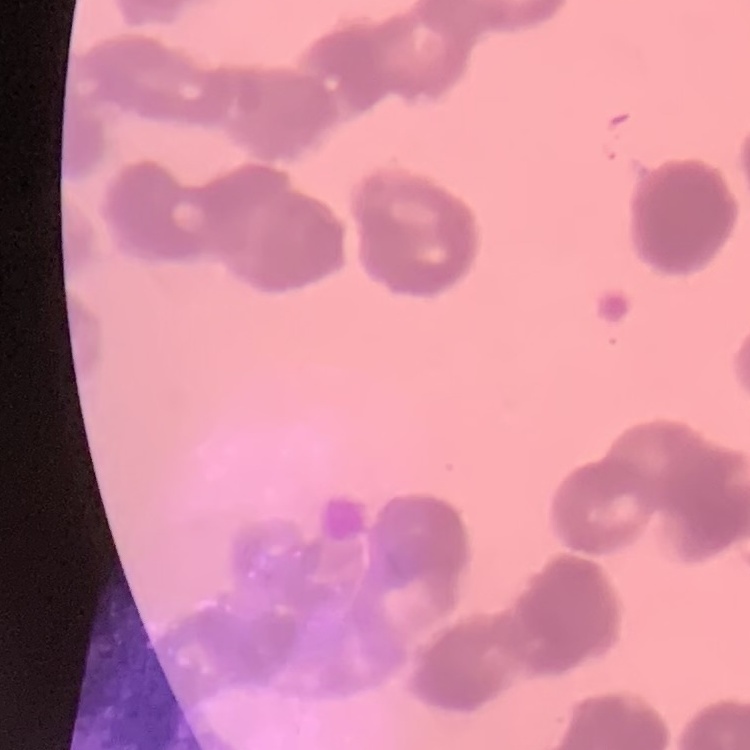 The red blood cells show rouleaux formation. One tile cut from a larger photomicrograph. Thin peripheral smear. Stained with either Field's or Giemsa.